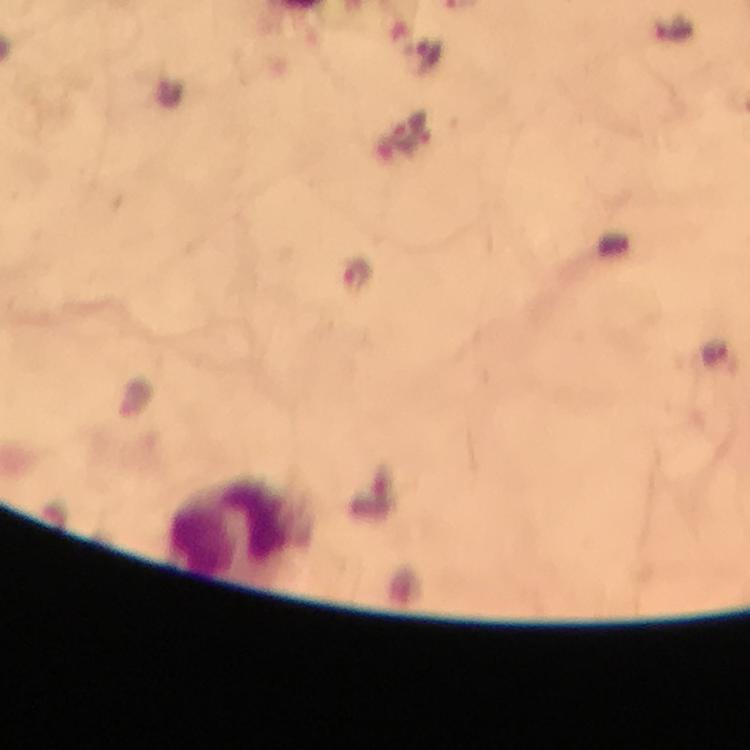
Approximate object centers, in pixels from the top-left corner. Leukocyte locations: (x=237, y=529). Image is 750×750 pixels. Thick blood film. Photographed through the microscope with a smartphone camera. Immersion oil applied. From a malaria diagnostic workup. Cropped region of a single field of view. Giemsa-stained preparation. Plasmodium parasites: none seen. 100x magnification.